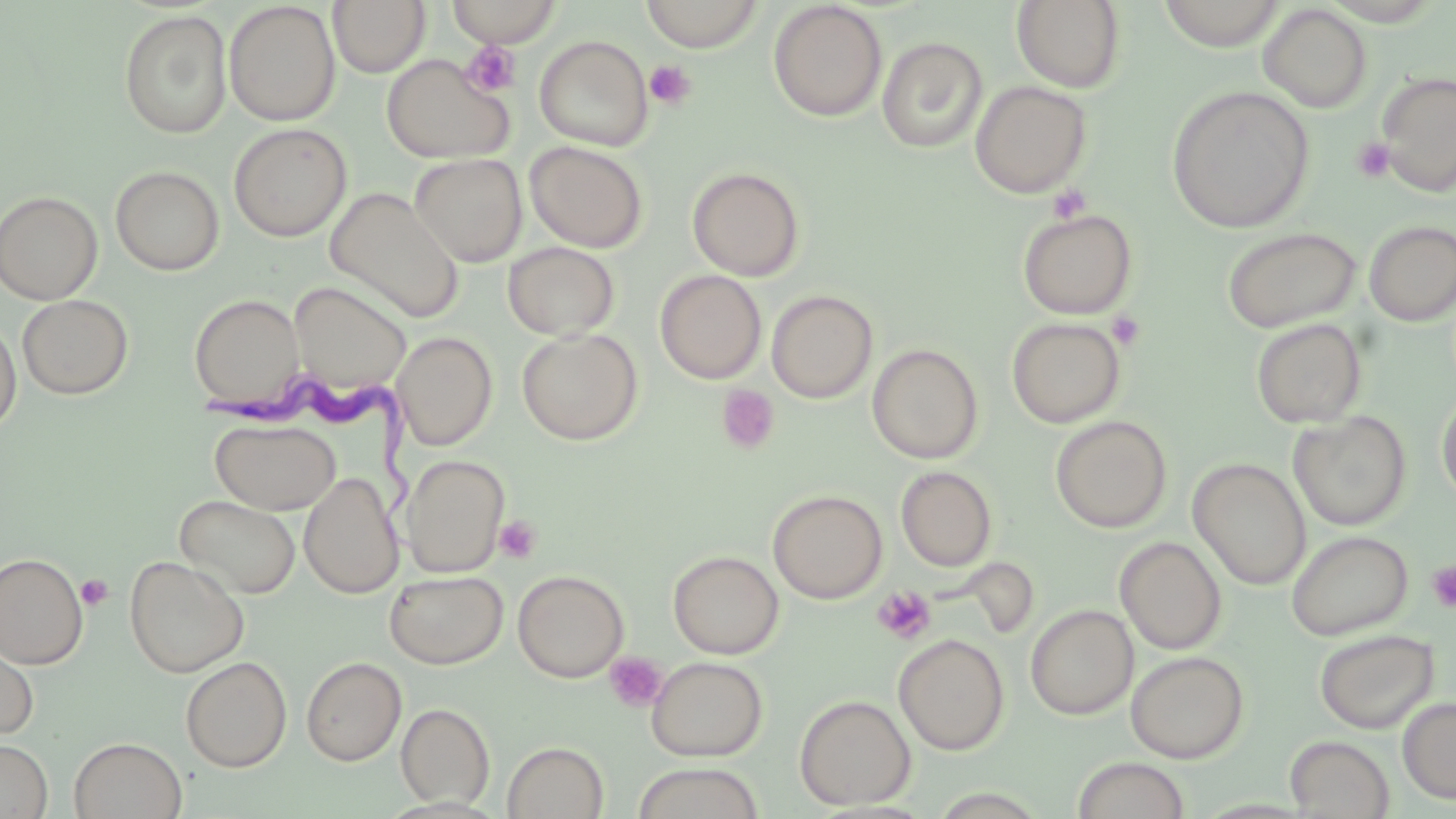
Approximate bounding boxes as (x1,y1)-(x2,y2) corner pairs in pixels. Platelet locations: (460,43)-(521,97), (645,60)-(696,110), (1351,137)-(1397,183), (1048,183)-(1092,223), (1106,311)-(1146,351), (717,385)-(780,455), (494,515)-(542,564), (1426,561)-(1456,613), (76,574)-(114,611), (872,586)-(936,645), (604,652)-(668,713). Trypanosoma brucei locations: (210,371)-(426,544). Uninfected red blood cell locations: (328,0)-(430,77), (446,0)-(562,47), (640,0)-(765,52), (1012,0)-(1126,92), (1156,0)-(1288,49), (1318,0)-(1449,26), (223,1)-(340,126), (768,2)-(887,122), (1258,4)-(1373,113), (119,10)-(232,139), (534,35)-(654,151), (877,36)-(988,153), (381,53)-(514,164), (1375,71)-(1456,196), (969,80)-(1092,199), (1167,86)-(1315,233), (229,123)-(351,242), (525,141)-(648,253), (409,153)-(528,267), (111,166)-(225,275), (687,166)-(805,281), (324,187)-(465,323), (0,190)-(104,305), (1017,208)-(1138,320), (1364,220)-(1456,326), (1221,226)-(1362,333), (502,242)-(620,340), (655,270)-(767,384), (289,282)-(410,395), (766,290)-(878,404), (189,293)-(305,409), (17,294)-(134,399), (0,314)-(22,435), (1007,317)-(1126,428), (1250,318)-(1367,428), (517,328)-(643,445), (392,331)-(497,450), (867,343)-(983,464), (1436,391)-(1456,507), (1288,411)-(1412,531), (1050,415)-(1172,533), (211,419)-(340,514), (401,454)-(510,577), (1189,458)-(1311,590), (896,466)-(997,571), (299,472)-(402,599), (767,489)-(887,604), (175,494)-(300,599), (1286,530)-(1414,640), (1115,536)-(1226,654), (668,550)-(783,659), (0,552)-(88,669), (124,555)-(250,677), (512,569)-(629,683), (384,570)-(508,669), (1025,604)-(1138,720), (1314,629)-(1439,734), (893,634)-(1010,755), (0,637)-(39,741), (1126,651)-(1249,764), (646,655)-(768,761), (180,656)-(292,772), (301,656)-(406,766), (794,694)-(916,810), (1397,697)-(1456,804), (396,703)-(495,809), (1284,735)-(1395,818), (69,736)-(187,819), (0,739)-(52,819), (502,741)-(608,819), (1071,757)-(1191,819), (631,762)-(765,819). Slide-level diagnosis: Trypanosoma brucei. May-Grünwald-Giemsa stain. Optical microscopy. Image is 1456×819 pixels. 1000x magnification. Thin blood film. One field of a larger specimen.